Assess this cell for malaria.
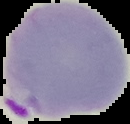

Parasitized.

image size = 130×124 pixels
preparation = thin blood smear
image type = segmented cell region on a black background